Identify the blood parasite species.
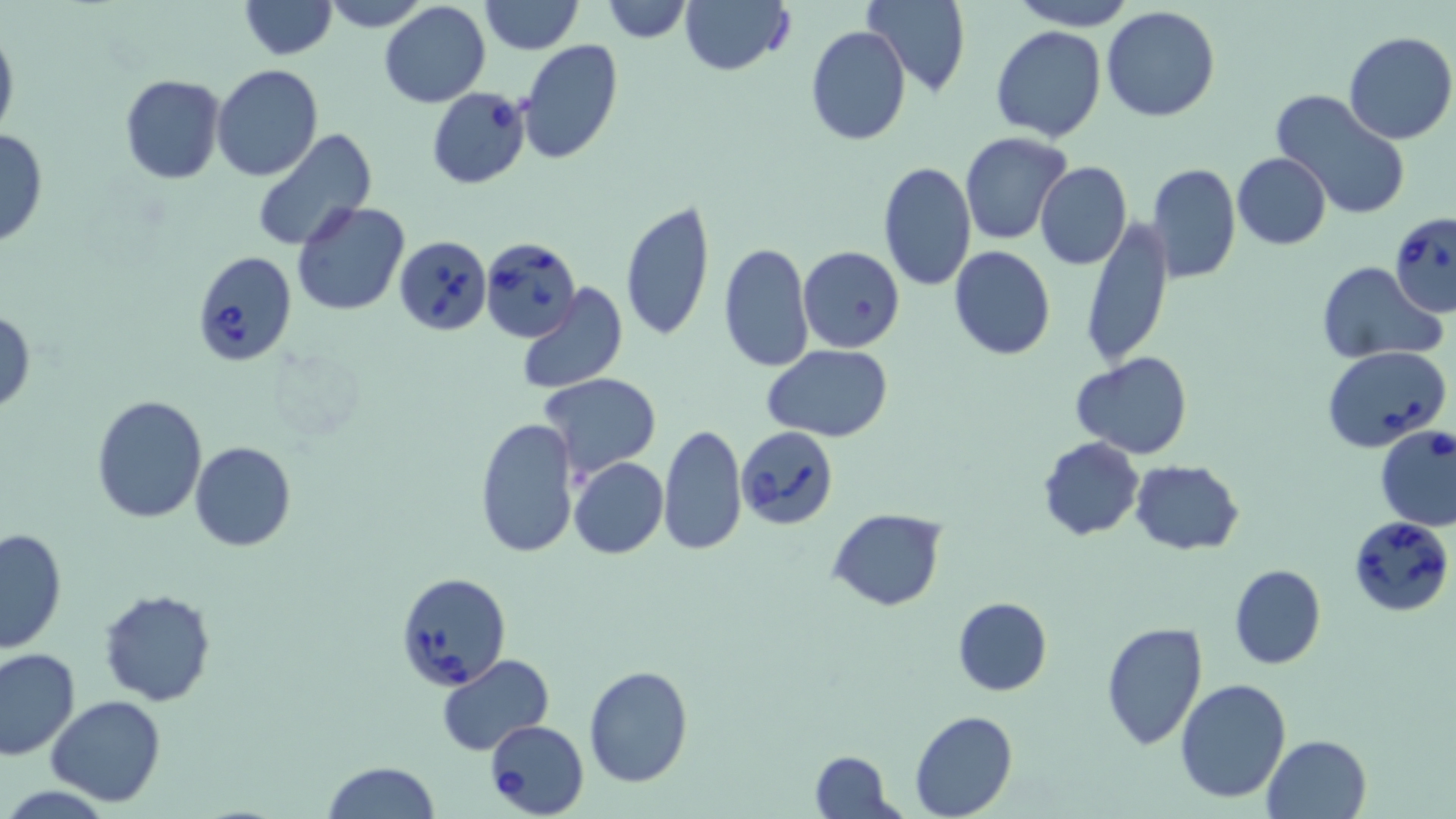
Babesia divergens.

Approximate bounding boxes as named x1/y1/x2/y2 corners in pixels. Uninfected red blood cell locations: (x1=241, y1=0, x2=336, y2=60), (x1=320, y1=0, x2=430, y2=31), (x1=479, y1=0, x2=581, y2=53), (x1=603, y1=0, x2=691, y2=43), (x1=679, y1=0, x2=794, y2=77), (x1=864, y1=0, x2=971, y2=97), (x1=1011, y1=0, x2=1136, y2=29), (x1=379, y1=2, x2=489, y2=108), (x1=1100, y1=6, x2=1220, y2=122), (x1=0, y1=25, x2=19, y2=143), (x1=805, y1=26, x2=911, y2=147), (x1=991, y1=26, x2=1107, y2=144), (x1=1342, y1=31, x2=1456, y2=145), (x1=518, y1=40, x2=624, y2=167), (x1=211, y1=65, x2=324, y2=182), (x1=119, y1=74, x2=226, y2=184), (x1=1270, y1=89, x2=1413, y2=221), (x1=0, y1=125, x2=49, y2=250), (x1=250, y1=130, x2=378, y2=250), (x1=959, y1=132, x2=1071, y2=245), (x1=1231, y1=152, x2=1331, y2=250), (x1=878, y1=161, x2=976, y2=291), (x1=1035, y1=162, x2=1131, y2=270), (x1=1146, y1=164, x2=1241, y2=284), (x1=620, y1=198, x2=716, y2=343), (x1=291, y1=199, x2=411, y2=315), (x1=1082, y1=217, x2=1172, y2=369), (x1=717, y1=242, x2=814, y2=373), (x1=799, y1=246, x2=905, y2=353), (x1=949, y1=246, x2=1056, y2=360), (x1=1317, y1=262, x2=1442, y2=365), (x1=518, y1=283, x2=629, y2=396), (x1=1, y1=308, x2=35, y2=415), (x1=761, y1=344, x2=893, y2=441), (x1=1070, y1=353, x2=1194, y2=457), (x1=539, y1=374, x2=661, y2=479), (x1=92, y1=393, x2=208, y2=523), (x1=475, y1=418, x2=579, y2=558), (x1=658, y1=423, x2=748, y2=557), (x1=1038, y1=437, x2=1144, y2=540), (x1=189, y1=441, x2=296, y2=552), (x1=569, y1=456, x2=669, y2=559), (x1=1130, y1=460, x2=1245, y2=555), (x1=828, y1=507, x2=947, y2=612), (x1=0, y1=527, x2=69, y2=653), (x1=1229, y1=564, x2=1326, y2=669), (x1=99, y1=588, x2=218, y2=707), (x1=952, y1=596, x2=1053, y2=696), (x1=1100, y1=622, x2=1209, y2=751), (x1=0, y1=647, x2=80, y2=760), (x1=437, y1=654, x2=556, y2=757), (x1=583, y1=664, x2=694, y2=787), (x1=1174, y1=679, x2=1291, y2=804), (x1=45, y1=695, x2=166, y2=807), (x1=909, y1=711, x2=1018, y2=819), (x1=1263, y1=735, x2=1372, y2=819), (x1=808, y1=750, x2=897, y2=819), (x1=321, y1=760, x2=439, y2=819). Babesia divergens-infected red blood cell locations: (x1=427, y1=88, x2=530, y2=189), (x1=1389, y1=212, x2=1456, y2=318), (x1=394, y1=235, x2=492, y2=335), (x1=481, y1=236, x2=581, y2=344), (x1=191, y1=251, x2=297, y2=368), (x1=1323, y1=346, x2=1449, y2=456), (x1=737, y1=425, x2=839, y2=530), (x1=1376, y1=427, x2=1455, y2=529), (x1=1349, y1=516, x2=1454, y2=617), (x1=396, y1=572, x2=512, y2=690), (x1=484, y1=721, x2=588, y2=817). Image is 1456×819 pixels. May-Grünwald-Giemsa stain. 1000x magnification. Single field of view. Thin blood smear. Optical microscopy.